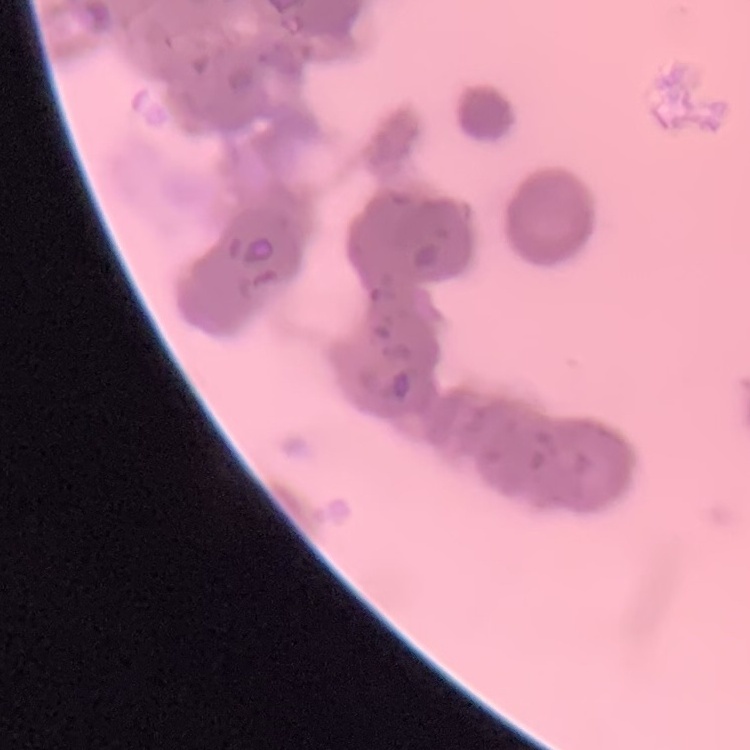

Summary:
  - Erythrocyte morphology: rouleaux formation
  - Image type: one tile cut from a larger photomicrograph
  - Preparation: thin blood smear
  - Stain: Field's or Giemsa